Find the red blood cells and label each as Plasmodium falciparum-infected, uninfected, or of indeterminate infection status.
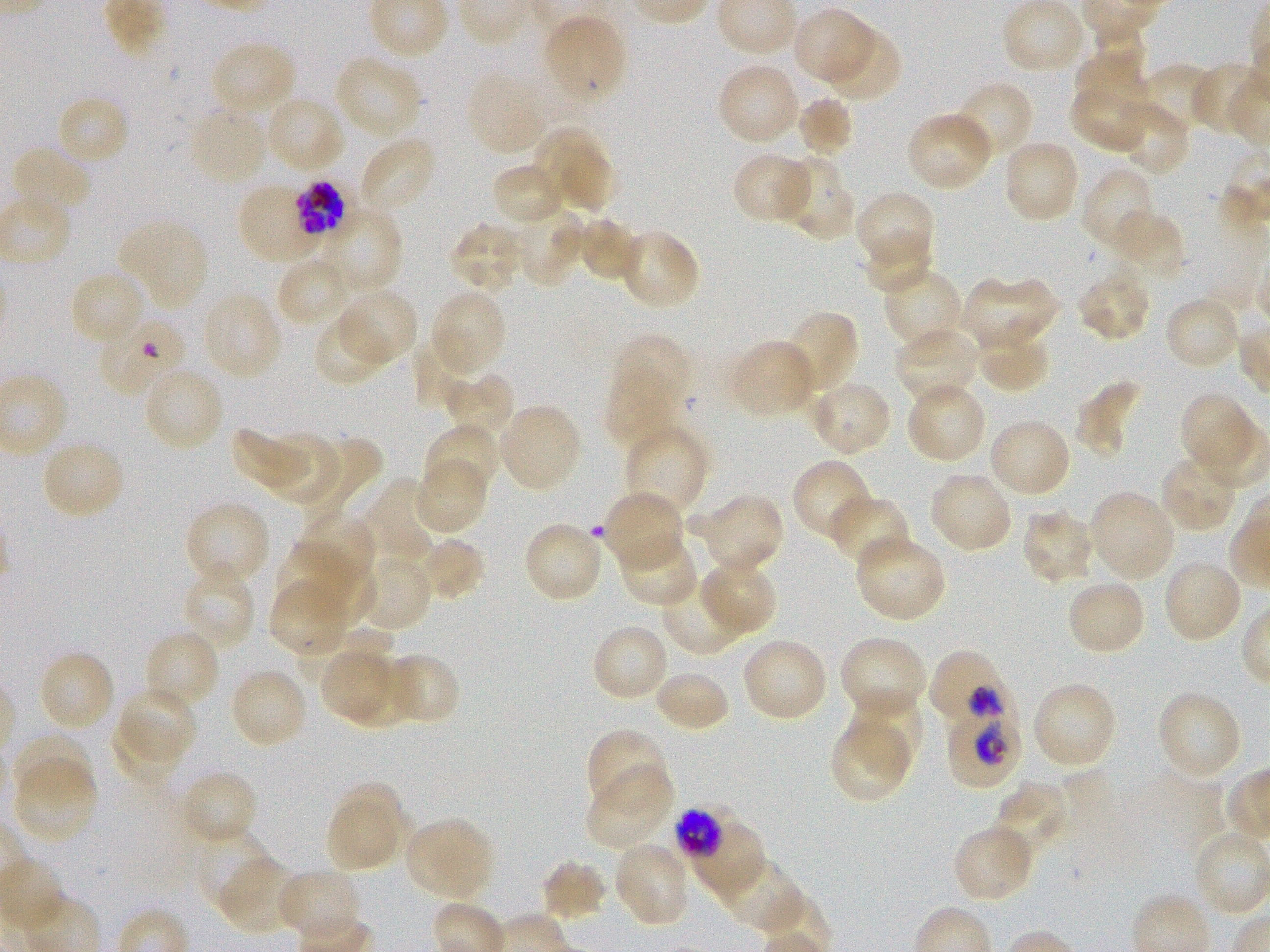

Approximate bounding rectangles given as corner coordinates in pixels from the top-left. Not every red blood cell is marked. A life-cycle stage — or a range of stages, where the recorded stages span more than one — follows each staged infected red blood cell.
Infected red blood cells: (x1=292, y1=179, x2=349, y2=238) late trophozoite to early schizont; (x1=928, y1=649, x2=1010, y2=730) trophozoite; (x1=945, y1=697, x2=1022, y2=789) trophozoite; (x1=674, y1=808, x2=725, y2=860) late trophozoite to late schizont.
Uninfected red blood cells: (x1=1003, y1=1, x2=1086, y2=75), (x1=792, y1=8, x2=874, y2=86), (x1=543, y1=15, x2=627, y2=103), (x1=823, y1=30, x2=902, y2=101), (x1=211, y1=40, x2=298, y2=117), (x1=1075, y1=40, x2=1148, y2=112), (x1=333, y1=55, x2=423, y2=139), (x1=1190, y1=61, x2=1263, y2=138), (x1=716, y1=63, x2=801, y2=145), (x1=1137, y1=63, x2=1215, y2=134), (x1=467, y1=69, x2=548, y2=155), (x1=954, y1=80, x2=1034, y2=161), (x1=1070, y1=82, x2=1149, y2=153), (x1=55, y1=95, x2=131, y2=167), (x1=795, y1=95, x2=855, y2=158), (x1=265, y1=96, x2=346, y2=175), (x1=1114, y1=100, x2=1190, y2=177), (x1=188, y1=104, x2=268, y2=186), (x1=905, y1=111, x2=994, y2=192), (x1=532, y1=128, x2=610, y2=209), (x1=358, y1=136, x2=437, y2=214), (x1=1002, y1=139, x2=1081, y2=223), (x1=10, y1=146, x2=93, y2=218), (x1=558, y1=151, x2=621, y2=217), (x1=731, y1=153, x2=813, y2=224), (x1=779, y1=156, x2=855, y2=242), (x1=490, y1=162, x2=566, y2=226), (x1=1081, y1=166, x2=1158, y2=253), (x1=238, y1=183, x2=320, y2=264), (x1=855, y1=190, x2=936, y2=271), (x1=319, y1=207, x2=403, y2=295), (x1=512, y1=208, x2=585, y2=287), (x1=1110, y1=209, x2=1186, y2=278), (x1=576, y1=216, x2=639, y2=283), (x1=117, y1=219, x2=209, y2=310), (x1=448, y1=220, x2=526, y2=293), (x1=617, y1=229, x2=702, y2=311), (x1=861, y1=233, x2=933, y2=295), (x1=275, y1=256, x2=353, y2=328), (x1=882, y1=268, x2=964, y2=354), (x1=1075, y1=268, x2=1151, y2=344), (x1=69, y1=271, x2=147, y2=348), (x1=962, y1=275, x2=1059, y2=350), (x1=336, y1=288, x2=419, y2=366), (x1=430, y1=289, x2=508, y2=374), (x1=201, y1=291, x2=284, y2=380), (x1=1164, y1=296, x2=1242, y2=372), (x1=784, y1=309, x2=861, y2=393), (x1=313, y1=314, x2=391, y2=387), (x1=98, y1=315, x2=188, y2=398), (x1=975, y1=326, x2=1052, y2=393), (x1=894, y1=328, x2=978, y2=406), (x1=609, y1=333, x2=692, y2=411), (x1=412, y1=336, x2=478, y2=410), (x1=727, y1=339, x2=817, y2=419), (x1=143, y1=366, x2=225, y2=452), (x1=604, y1=371, x2=681, y2=450), (x1=441, y1=372, x2=515, y2=444), (x1=1075, y1=380, x2=1142, y2=458), (x1=808, y1=381, x2=893, y2=457), (x1=905, y1=382, x2=987, y2=465), (x1=1179, y1=391, x2=1254, y2=466), (x1=498, y1=403, x2=583, y2=492), (x1=987, y1=418, x2=1073, y2=498), (x1=423, y1=423, x2=500, y2=500), (x1=622, y1=424, x2=708, y2=518), (x1=232, y1=427, x2=311, y2=493), (x1=268, y1=433, x2=342, y2=506), (x1=310, y1=434, x2=383, y2=518), (x1=41, y1=439, x2=125, y2=521), (x1=1159, y1=454, x2=1238, y2=533), (x1=792, y1=459, x2=875, y2=543), (x1=416, y1=461, x2=487, y2=534), (x1=928, y1=472, x2=1013, y2=555), (x1=358, y1=477, x2=437, y2=565), (x1=603, y1=489, x2=684, y2=573), (x1=1088, y1=490, x2=1175, y2=581), (x1=684, y1=494, x2=784, y2=575), (x1=828, y1=495, x2=911, y2=569), (x1=183, y1=501, x2=271, y2=587), (x1=1021, y1=509, x2=1096, y2=586), (x1=295, y1=511, x2=377, y2=587), (x1=522, y1=522, x2=605, y2=604), (x1=618, y1=534, x2=700, y2=608), (x1=855, y1=534, x2=948, y2=623), (x1=417, y1=536, x2=486, y2=602), (x1=276, y1=543, x2=355, y2=616), (x1=296, y1=550, x2=376, y2=623), (x1=357, y1=555, x2=433, y2=633), (x1=698, y1=558, x2=779, y2=637), (x1=1162, y1=558, x2=1244, y2=643), (x1=180, y1=566, x2=257, y2=651), (x1=662, y1=578, x2=749, y2=655), (x1=268, y1=579, x2=350, y2=656), (x1=1065, y1=579, x2=1147, y2=657), (x1=590, y1=623, x2=670, y2=704), (x1=296, y1=626, x2=394, y2=685), (x1=144, y1=629, x2=220, y2=712), (x1=839, y1=635, x2=927, y2=720), (x1=740, y1=637, x2=830, y2=722), (x1=37, y1=649, x2=116, y2=733), (x1=319, y1=650, x2=393, y2=719), (x1=384, y1=652, x2=461, y2=722), (x1=347, y1=658, x2=420, y2=727), (x1=229, y1=667, x2=308, y2=750), (x1=654, y1=669, x2=731, y2=734), (x1=1031, y1=680, x2=1117, y2=769), (x1=117, y1=684, x2=196, y2=763), (x1=1155, y1=689, x2=1243, y2=781), (x1=850, y1=690, x2=923, y2=772), (x1=829, y1=717, x2=911, y2=804), (x1=112, y1=721, x2=183, y2=785), (x1=585, y1=728, x2=670, y2=813), (x1=12, y1=735, x2=92, y2=806), (x1=14, y1=763, x2=98, y2=844), (x1=584, y1=768, x2=672, y2=850), (x1=180, y1=769, x2=259, y2=846), (x1=338, y1=781, x2=414, y2=859), (x1=994, y1=781, x2=1070, y2=856), (x1=327, y1=802, x2=398, y2=871), (x1=688, y1=816, x2=766, y2=900), (x1=404, y1=817, x2=495, y2=900), (x1=952, y1=824, x2=1036, y2=904), (x1=195, y1=829, x2=273, y2=912), (x1=612, y1=841, x2=692, y2=926), (x1=715, y1=853, x2=805, y2=933), (x1=219, y1=857, x2=302, y2=935), (x1=540, y1=860, x2=608, y2=922), (x1=277, y1=868, x2=362, y2=942).
No red blood cells of indeterminate infection status observed.

culture = static in-vitro Plasmodium falciparum strain 3D7
stain = Giemsa
preparation = thin blood film
image size = 1270×952 pixels
objective = 100x, oil immersion, numerical aperture 1.25
field of view = single
donor blood group = O+